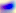
magnification: 400x
identification: Toxoplasma gondii
modality: photomicrograph